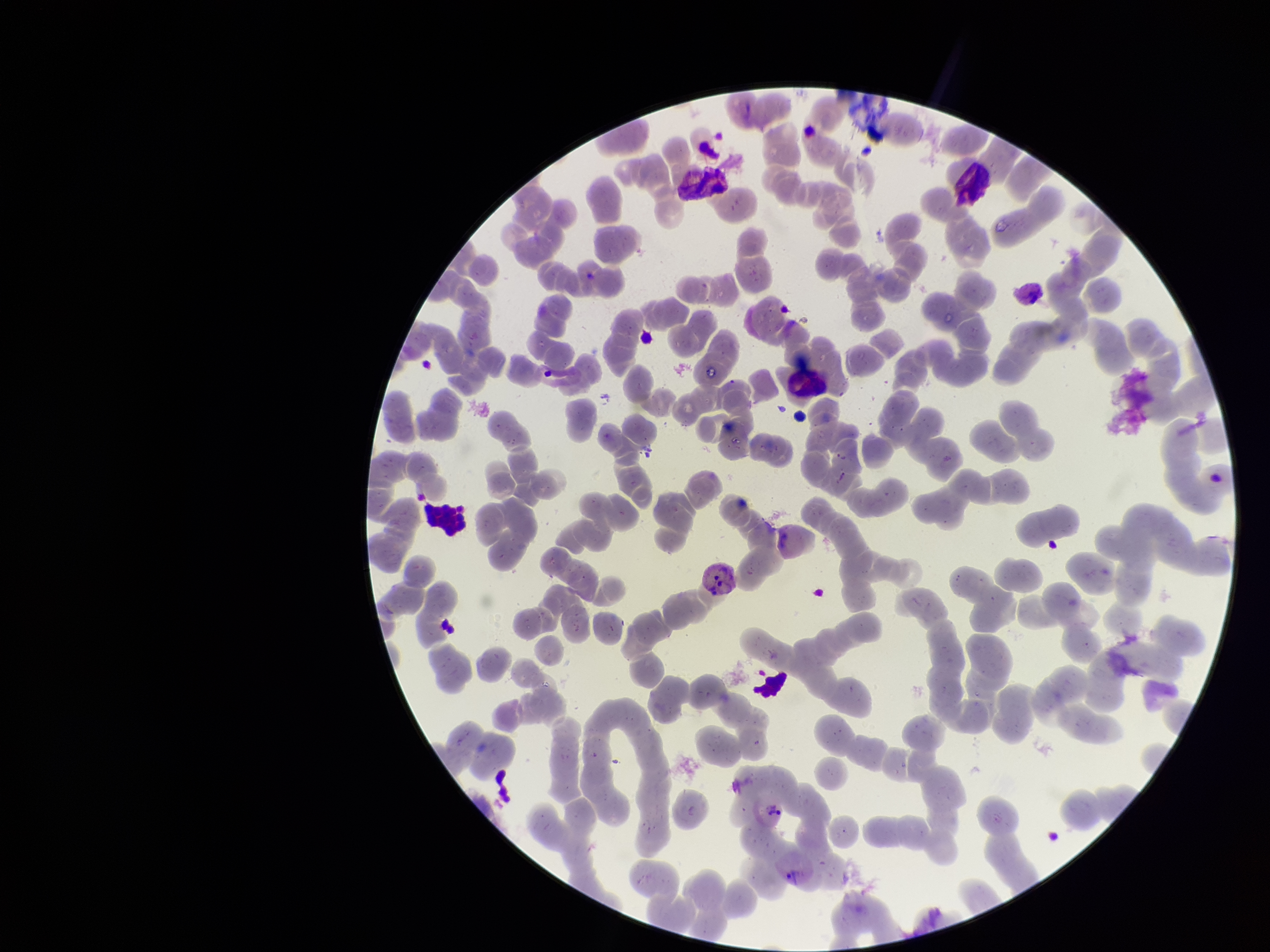

One field from this slide. Parasitized red blood cell count: 2. Parasitized red blood cells: detected. Photographed through the microscope eyepiece with a smartphone camera. Red blood cell count: 243. Preparation: thin. Stained with Giemsa. Patient malaria status: positive. Image is 1270×952 pixels. Species reported for this patient: Plasmodium vivax.